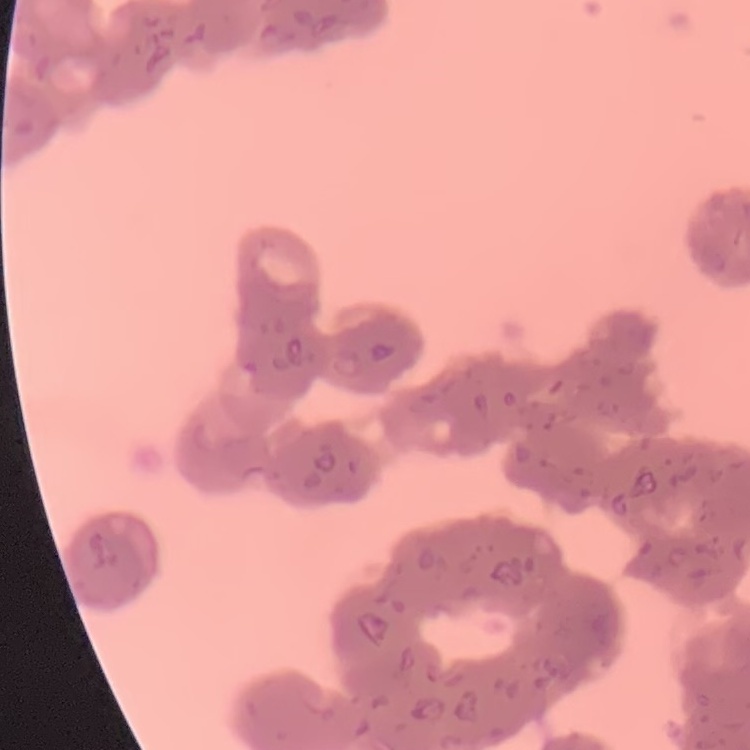

Summary:
  - Erythrocyte morphology: rouleaux formation
  - Preparation: thin blood smear
  - Stain: Field's or Giemsa
  - Image type: one tile cut from a larger photomicrograph